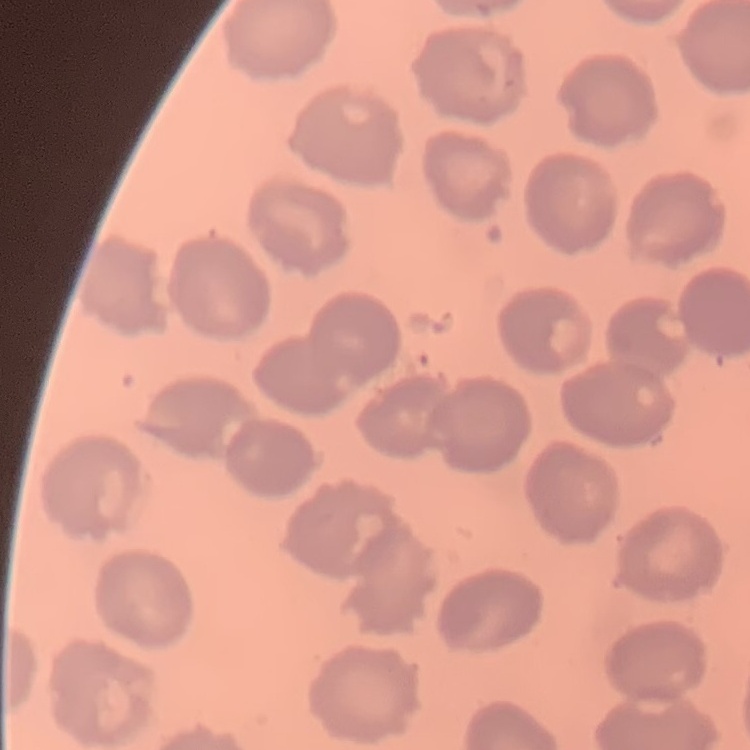
The erythrocytes exhibit no rouleaux formation. Thin blood film. Square crop of a larger photomicrograph. Field's or Giemsa stain.